Report the malaria status of this cell.
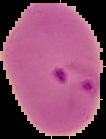

It is parasitized.

Summary:
  - Preparation: thin blood smear
  - Image type: cell region segmented out of the field of view; surrounding area masked to black
  - Image size: 106×139 pixels